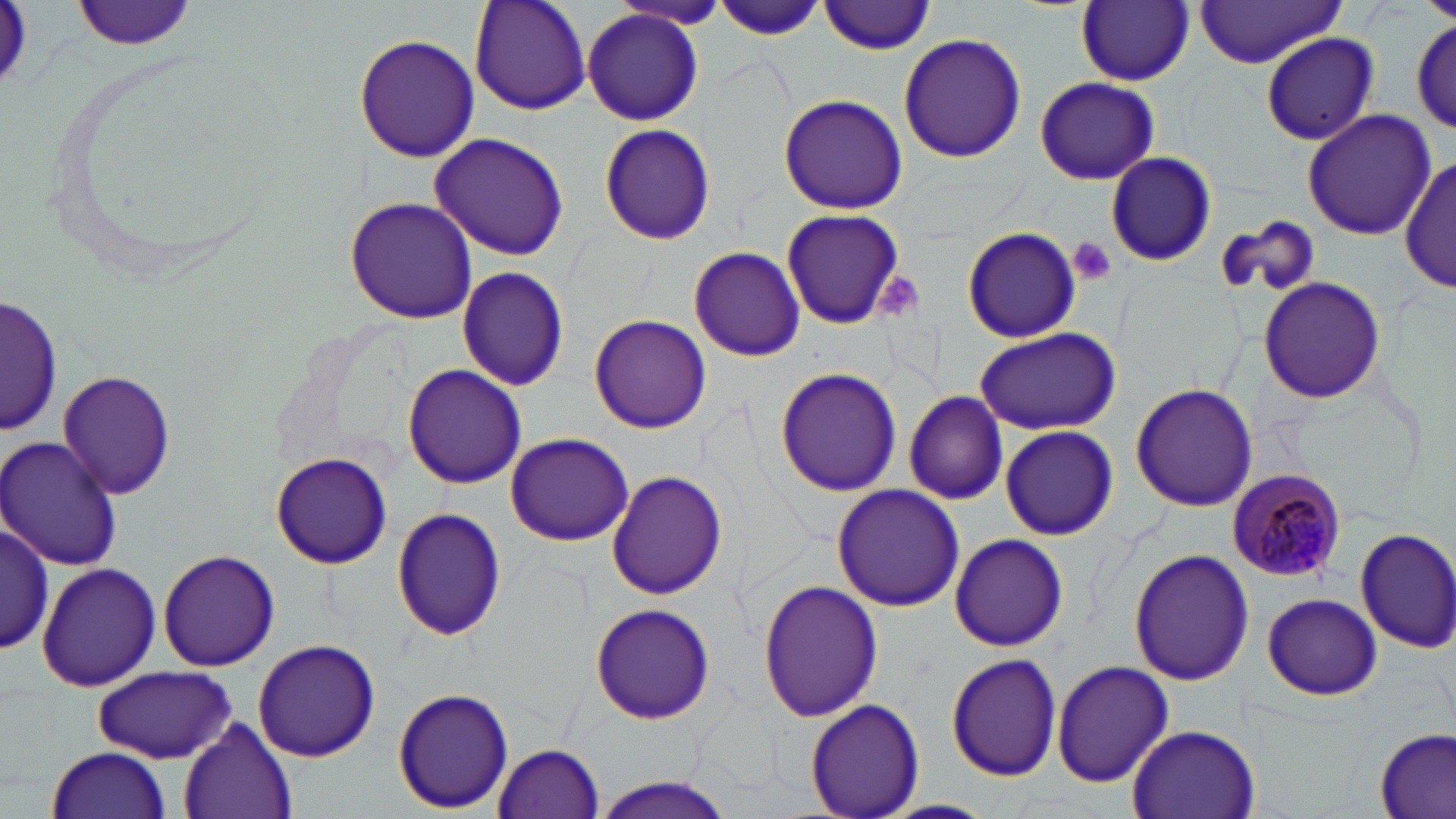

Summary:
  - Coordinate format: approximate bounding boxes as [x1, y1, x2, y2] in pixels
  - Plasmodium malariae-infected red blood cell locations: [1226, 468, 1346, 581]
  - Uninfected red blood cell locations: [73, 0, 197, 51], [469, 0, 591, 116], [819, 0, 939, 55], [711, 1, 830, 40], [1077, 1, 1194, 86], [1189, 2, 1350, 67], [581, 8, 705, 127], [1411, 18, 1454, 133], [353, 31, 479, 163], [898, 31, 1026, 163], [1259, 32, 1380, 146], [1034, 76, 1159, 185], [776, 94, 909, 214], [1302, 108, 1435, 240], [598, 124, 717, 246], [429, 133, 570, 260], [1104, 152, 1215, 268], [1399, 155, 1456, 296], [344, 196, 478, 321], [779, 207, 907, 330], [1216, 216, 1319, 299], [961, 226, 1083, 344], [688, 245, 806, 361], [456, 267, 570, 392], [1257, 276, 1385, 402], [1, 292, 60, 433], [589, 315, 710, 433], [973, 326, 1121, 435], [403, 363, 528, 487], [774, 367, 903, 498], [58, 370, 177, 500], [1131, 381, 1257, 513], [902, 390, 1009, 505], [999, 425, 1120, 537], [504, 431, 634, 544], [2, 434, 124, 571], [271, 452, 394, 569], [606, 470, 728, 600], [832, 484, 963, 612], [390, 506, 507, 640], [0, 518, 56, 656], [1354, 526, 1456, 652], [950, 533, 1067, 651], [1127, 547, 1255, 686], [158, 550, 281, 671], [37, 562, 159, 692], [757, 578, 883, 724], [1261, 593, 1383, 701], [589, 604, 718, 725], [252, 638, 380, 760], [947, 651, 1063, 781], [1051, 660, 1174, 787], [93, 667, 238, 762], [392, 686, 515, 813], [805, 700, 926, 819], [178, 716, 297, 819], [1126, 724, 1260, 819], [1375, 727, 1454, 819], [492, 742, 606, 819], [45, 746, 173, 819], [589, 777, 738, 818], [878, 800, 999, 819]
  - Platelet locations: [1068, 238, 1118, 287], [877, 274, 926, 319]
  - Slide-level diagnosis: Plasmodium malariae
  - Modality: light microscopy
  - Field of view: single
  - Magnification: 1000x
  - Image size: 1456×819 pixels
  - Preparation: thin blood smear
  - Stain: May-Grünwald-Giemsa